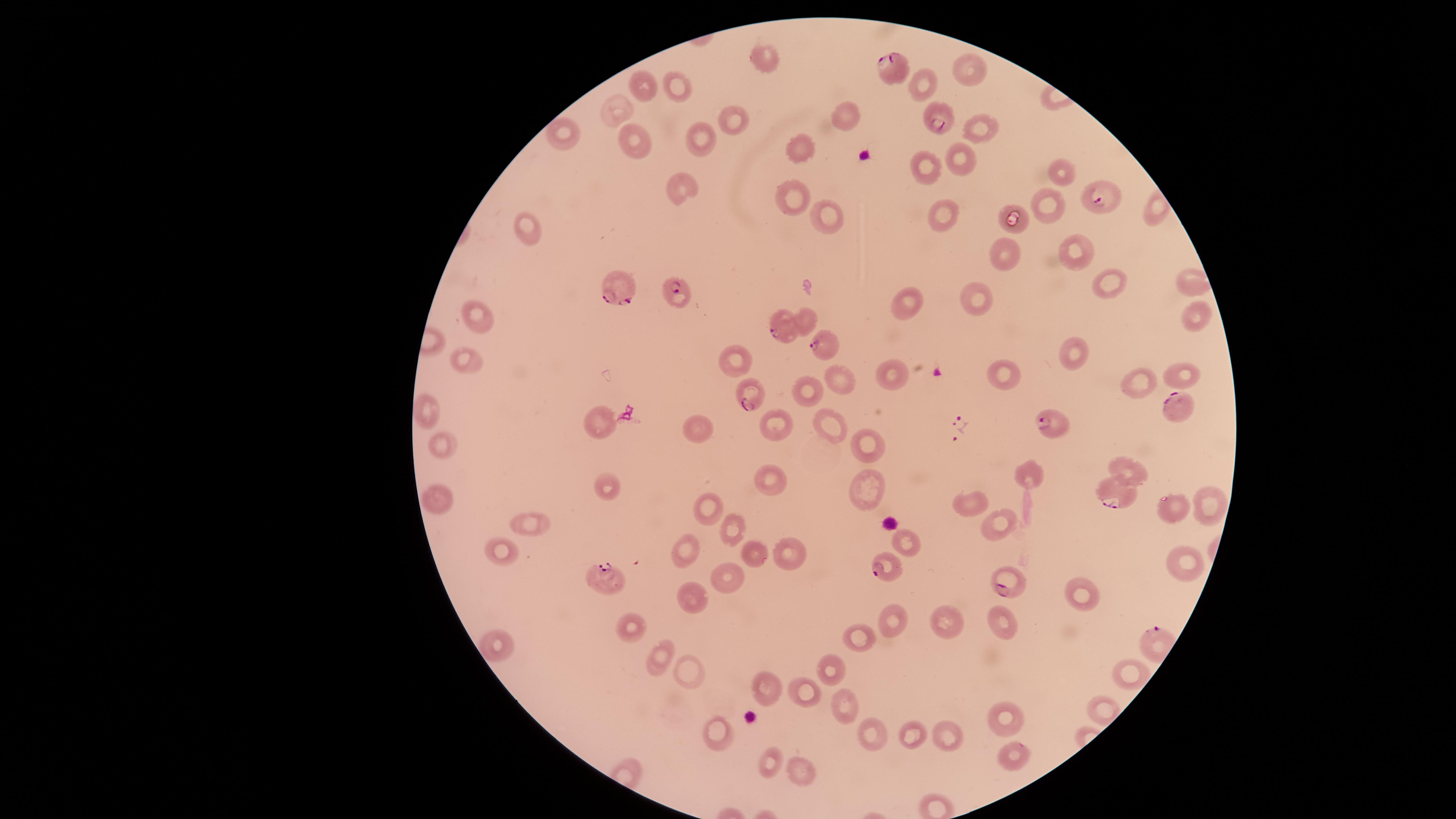

Approximate marker points as (x, y) in pixels.
Summary:
  - Uninfected RBCs: (759, 58), (970, 68), (642, 83), (920, 83), (676, 86), (613, 108), (847, 111), (730, 122), (978, 125), (562, 132), (632, 137), (698, 142), (801, 149), (957, 157), (926, 170), (1057, 171), (680, 187), (792, 193), (1051, 204), (942, 212), (828, 215), (1019, 221), (525, 228), (1076, 243), (1007, 253), (1186, 279), (1107, 282), (905, 302), (980, 302), (479, 312), (1196, 312), (807, 316), (1069, 353), (737, 360), (462, 365), (999, 374), (1182, 374), (891, 376), (840, 380), (1133, 381), (802, 394), (429, 412), (597, 422), (829, 422), (775, 424), (701, 425), (442, 442), (865, 443), (1132, 470), (1032, 473), (770, 479), (611, 483), (866, 489), (438, 491), (974, 504), (1202, 504), (709, 507), (1168, 508), (527, 524), (1004, 525), (731, 531), (906, 544), (684, 546), (501, 550), (748, 554), (790, 554), (1179, 560), (731, 578), (1081, 592), (689, 595), (1007, 619), (889, 620), (948, 624), (634, 629), (864, 640), (492, 643), (661, 656), (832, 671), (689, 672), (1128, 673), (765, 682), (801, 690), (843, 702), (1003, 718), (914, 729), (870, 732), (950, 735), (721, 737), (1012, 753), (767, 763), (800, 768)
  - Parasitized RBCs: (891, 69), (938, 120), (1102, 200), (622, 289), (678, 293), (783, 326), (823, 344), (753, 388), (1175, 407), (1053, 425), (1112, 497), (887, 568), (1010, 576), (600, 578)
  - Presence: malaria parasites detected
  - Field of view: single
  - Capture: smartphone photograph through the microscope eyepiece
  - Stain: Giemsa
  - Species: Plasmodium falciparum
  - Visible region: circular
  - Image size: 1456×819 pixels
  - Preparation: thin blood smear